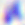 Captured at 400x magnification. Photomicrograph. Toxoplasma gondii is seen.